Locate every blood parasite and identify its species.
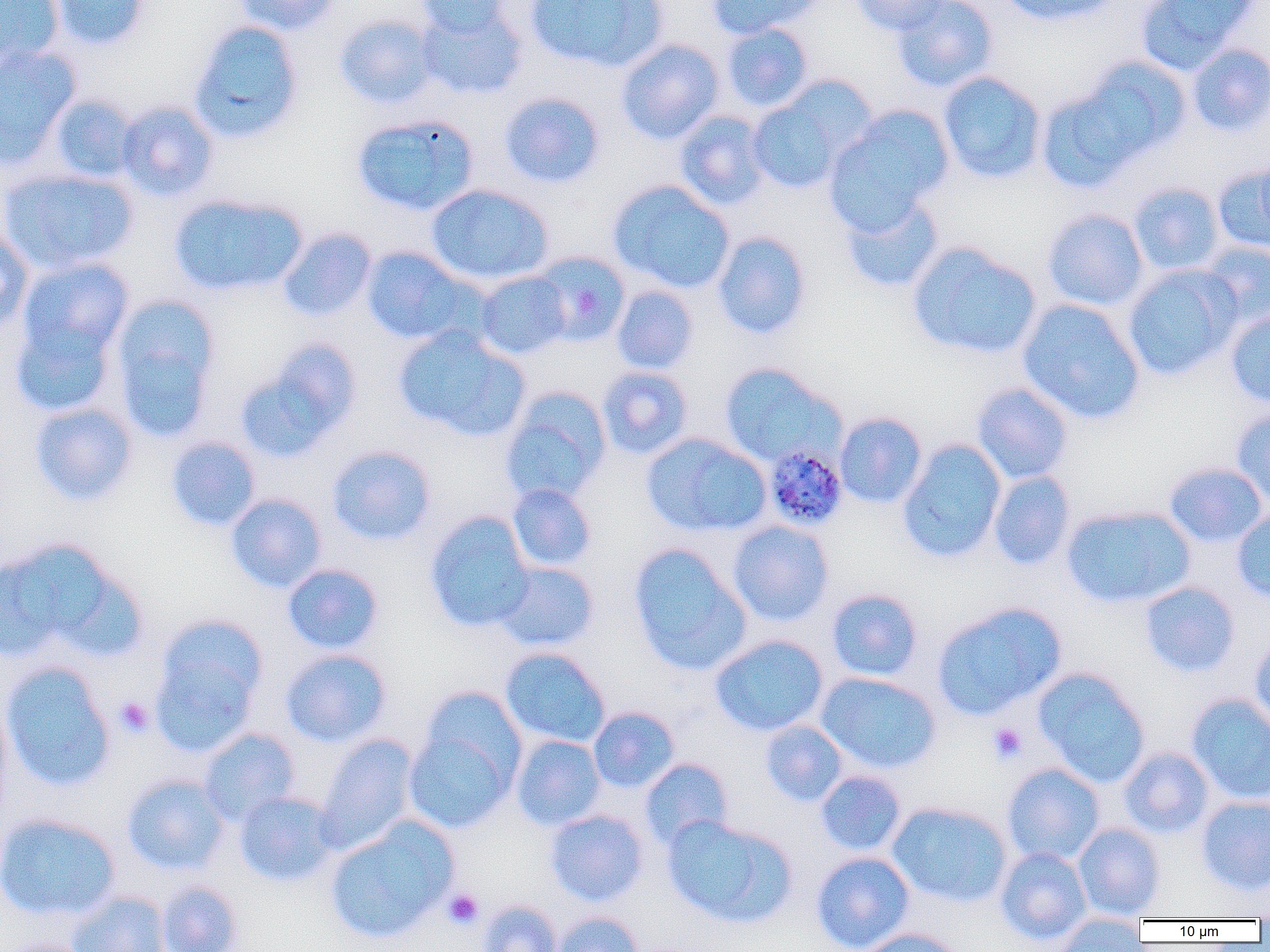
Approximate bounding boxes as (x1,y1)-(x2,y2) corner pairs in pixels.
Plasmodium malariae-infected red blood cells: (762,444)-(849,532).
No Plasmodium falciparum, Plasmodium ovale, Plasmodium vivax, Babesia divergens, or Trypanosoma brucei observed.

Summary:
  - Platelet locations: (115,697)-(155,738), (987,722)-(1028,765), (443,888)-(484,930)
  - Uninfected red blood cell locations: (0,0)-(65,68), (48,0)-(152,50), (231,0)-(343,36), (416,0)-(514,38), (525,0)-(667,73), (706,0)-(820,40), (851,0)-(953,36), (890,0)-(998,93), (998,0)-(1119,27), (1135,0)-(1255,73), (416,6)-(528,100), (334,13)-(439,109), (188,20)-(305,143), (721,23)-(813,112), (616,39)-(724,144), (1187,43)-(1270,137), (0,45)-(81,168), (1081,55)-(1192,157), (938,71)-(1046,183), (1036,85)-(1149,194), (746,89)-(857,194), (499,91)-(606,188), (48,94)-(141,183), (116,100)-(220,202), (825,107)-(952,231), (674,110)-(772,210), (351,113)-(480,216), (1255,154)-(1270,246), (1213,165)-(1270,254), (1,167)-(139,274), (608,180)-(736,294), (1129,182)-(1226,276), (426,183)-(555,286), (168,192)-(308,298), (839,193)-(945,293), (1042,208)-(1149,311), (0,228)-(34,339), (277,228)-(377,323), (711,231)-(812,340), (907,242)-(1042,361), (1199,242)-(1270,332), (361,245)-(473,346), (530,251)-(631,347), (15,257)-(135,370), (1122,264)-(1240,381), (474,271)-(571,359), (612,285)-(698,374), (110,295)-(221,440), (1017,299)-(1145,425), (10,309)-(120,418), (1224,310)-(1270,409), (393,325)-(530,441), (237,340)-(363,461), (718,362)-(841,467), (595,366)-(694,460), (972,381)-(1074,484), (500,388)-(611,505), (29,402)-(138,506), (1231,409)-(1270,508), (835,412)-(928,509), (642,432)-(771,538), (165,436)-(262,531), (897,439)-(1007,564), (326,444)-(437,546), (1163,462)-(1268,548), (989,470)-(1075,571), (506,483)-(597,572), (225,493)-(327,592), (1061,505)-(1195,609), (1231,506)-(1270,602), (424,511)-(536,633), (728,520)-(834,626), (0,542)-(108,660), (627,543)-(752,676), (493,561)-(600,651), (281,563)-(384,655), (1139,581)-(1241,678), (826,588)-(923,681), (932,601)-(1066,720), (151,620)-(267,752), (709,634)-(829,736), (1249,636)-(1270,734), (499,647)-(611,748), (280,648)-(392,748), (1,661)-(116,792), (1033,667)-(1151,787), (816,672)-(942,774), (417,685)-(528,787), (1187,693)-(1270,805), (0,696)-(14,824), (588,706)-(680,793), (760,720)-(848,806), (198,728)-(301,826), (403,728)-(516,833), (315,733)-(420,853), (511,735)-(606,830), (1119,747)-(1215,838), (640,758)-(733,849), (1002,763)-(1105,865), (815,770)-(906,856), (121,772)-(231,875), (234,791)-(340,887), (1197,795)-(1270,895), (887,801)-(1013,907), (545,809)-(649,906), (0,813)-(121,921), (661,814)-(797,928), (324,818)-(458,945), (1073,822)-(1166,919), (995,846)-(1092,945), (810,851)-(916,952), (156,880)-(244,952), (67,890)-(170,952), (477,900)-(562,952), (550,911)-(644,952), (1053,913)-(1149,951), (854,927)-(970,952), (3,938)-(100,952)
  - Slide-level diagnosis: Plasmodium malariae
  - Modality: light microscopy
  - Preparation: thin blood smear
  - Magnification: 1000x
  - Field of view: single
  - Image size: 1270×952 pixels